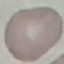

Malaria status: uninfected. Acquired by smartphone through the microscope eyepiece. Cell patch, automatically extracted from a larger field of view and resized to 64 × 64 pixels. Thin blood smear. Giemsa stain.